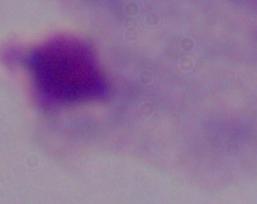
A trichomonad is shown. Photomicrograph. Captured at 1000x magnification.